Classify this cell by malaria status.
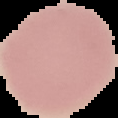

It is uninfected.

image size = 118×118 pixels
preparation = thin blood film
image type = segmented cell region with the area outside set to black